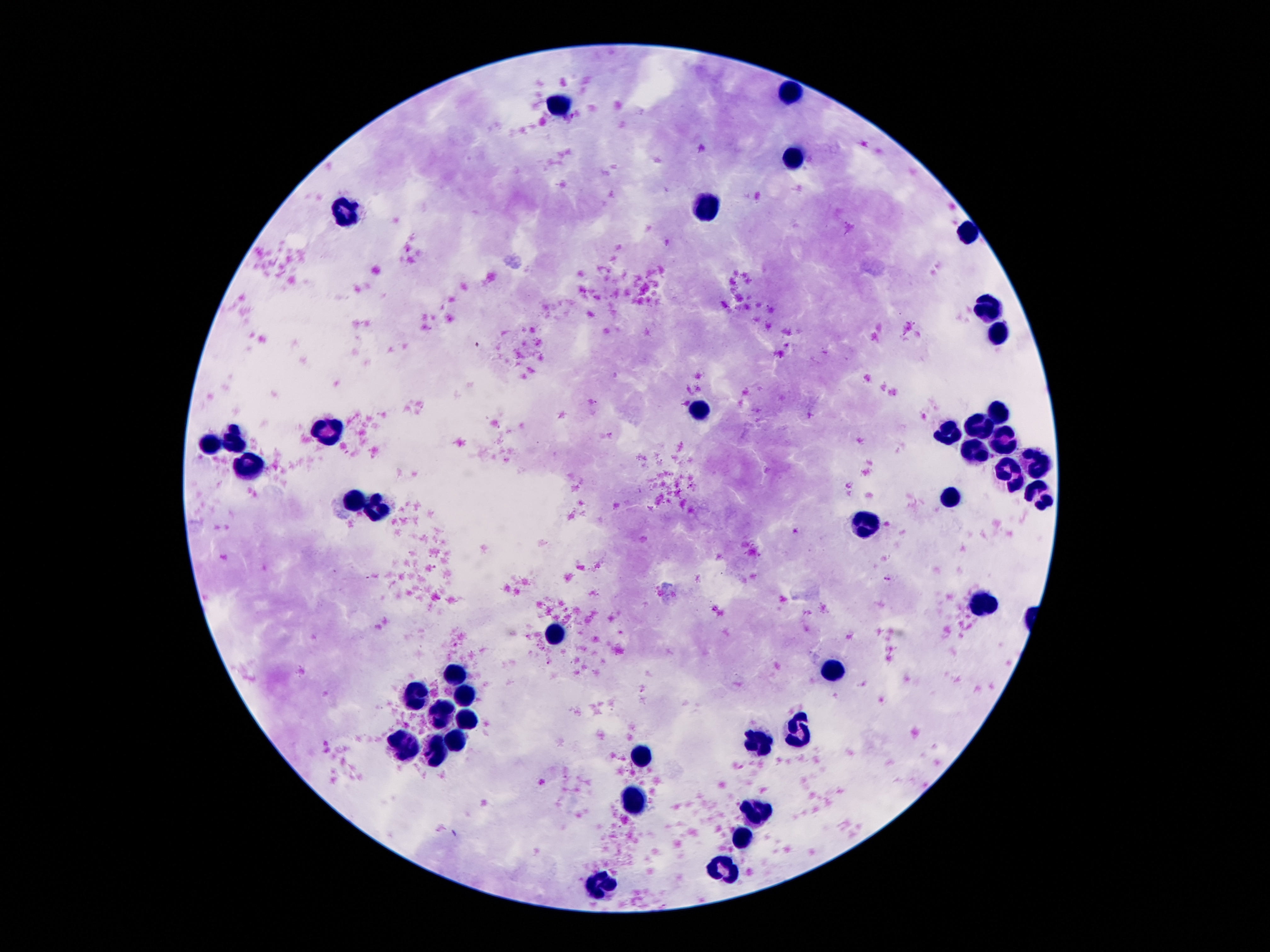

Approximate centers as {x, y} in pixels.
Summary:
  - Leukocyte locations: {790, 92}, {558, 101}, {796, 159}, {708, 206}, {347, 210}, {966, 233}, {989, 305}, {999, 335}, {698, 405}, {999, 411}, {976, 427}, {952, 431}, {337, 432}, {234, 442}, {212, 443}, {1007, 445}, {970, 452}, {247, 466}, {1036, 466}, {1007, 477}, {1038, 493}, {952, 498}, {351, 501}, {382, 511}, {864, 524}, {980, 608}, {554, 636}, {839, 672}, {456, 674}, {417, 698}, {460, 700}, {443, 714}, {466, 721}, {800, 733}, {456, 739}, {761, 746}, {406, 748}, {437, 750}, {642, 755}, {638, 797}, {759, 811}, {743, 835}, {728, 868}, {607, 882}
  - Image size: 1270×952 pixels
  - Preparation: thick blood film
  - Field of view: one from this slide
  - Capture: smartphone camera through the microscope eyepiece
  - Magnification: 100x
  - Patient malaria status: not infected
  - Stain: Giemsa